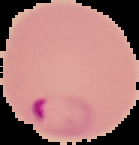

The area outside the segmented cell region is set to black. Image is 139×145 pixels. From a thin blood smear. Malaria status: parasitized.